State which parasite is depicted.
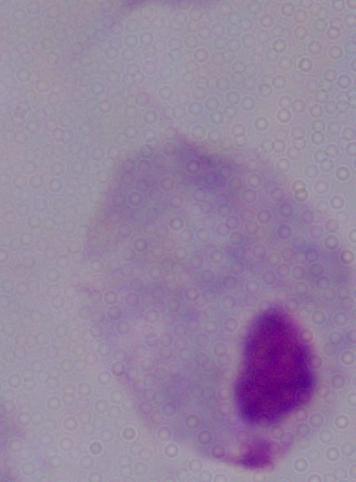
A trichomonad.

Summary:
  - Modality: photomicrograph
  - Magnification: 1000x